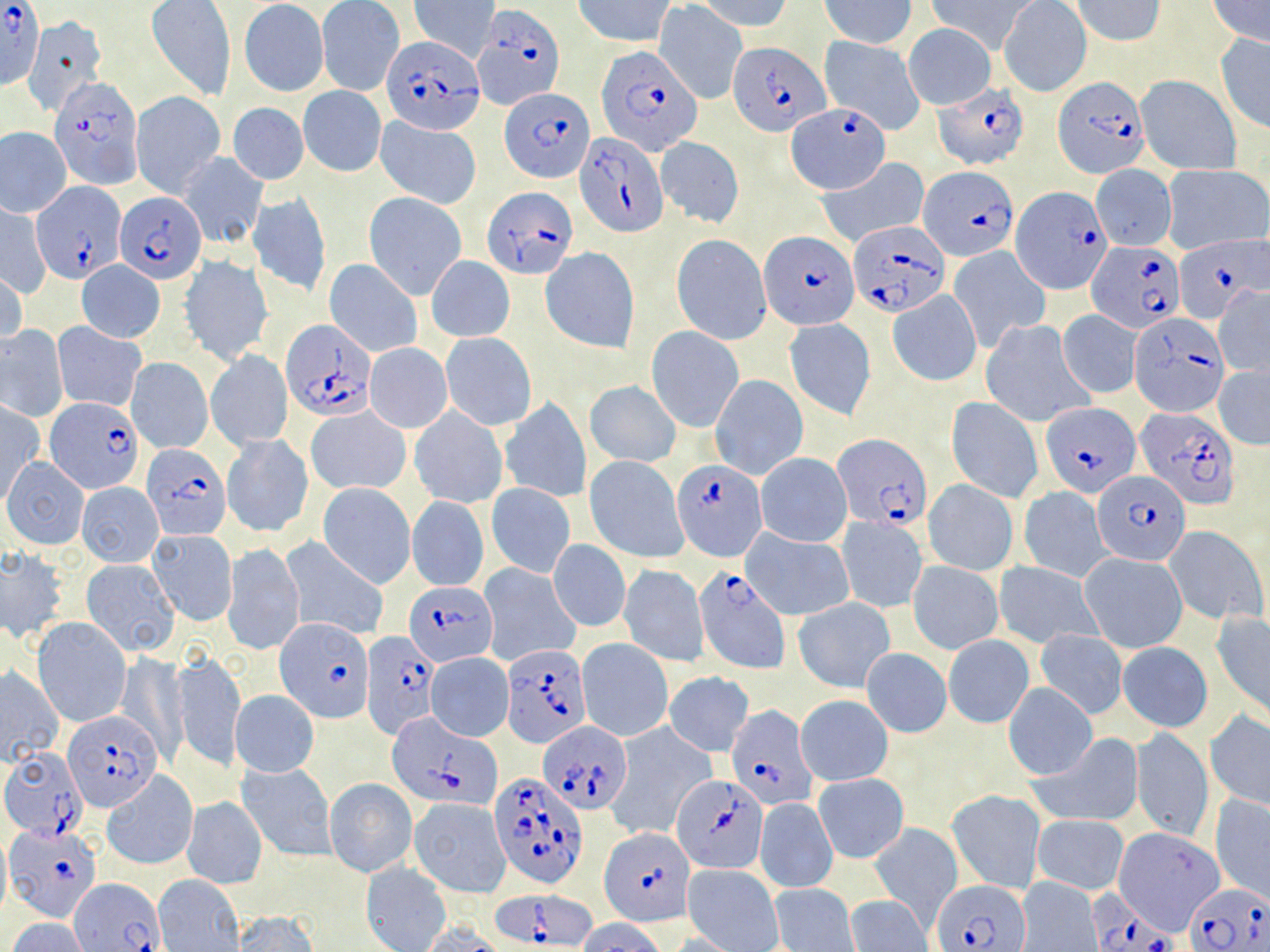
Summary:
  - Coordinate format: approximate bounding boxes as (x1,y1)-(x2,y2) corner pairs in pixels
  - Uninfected red blood cell locations (subset): (410,0)-(500,63), (572,0)-(677,48), (1071,0)-(1165,46), (1204,0)-(1270,48), (696,1)-(793,34), (822,1)-(917,48), (926,1)-(1038,55), (998,1)-(1092,97), (147,2)-(236,101), (240,2)-(329,96), (316,2)-(403,96), (656,4)-(748,104), (23,15)-(108,116), (903,24)-(996,110), (1214,33)-(1270,134), (820,35)-(926,134), (1137,74)-(1242,173), (298,86)-(386,177), (130,91)-(226,199), (228,102)-(308,186), (377,117)-(480,208), (1,127)-(71,215), (655,135)-(745,227), (178,152)-(268,249), (816,158)-(929,247), (1162,163)-(1269,255), (1090,164)-(1175,251), (248,192)-(331,298), (364,192)-(466,300), (1,204)-(51,299), (672,233)-(771,344), (540,246)-(638,353), (949,246)-(1050,348), (181,255)-(272,365), (427,258)-(514,342), (324,259)-(423,358), (76,260)-(165,344), (0,267)-(26,355), (1214,284)-(1270,379), (888,291)-(981,386), (1057,310)-(1142,397), (784,319)-(875,420), (981,319)-(1095,428), (53,323)-(145,411), (0,326)-(68,422), (646,326)-(743,432), (440,332)-(537,429), (365,343)-(452,433), (205,350)-(292,451), (126,357)-(213,454), (1213,365)-(1270,450), (710,374)-(808,482), (585,380)-(681,468), (499,396)-(591,503), (946,396)-(1043,503), (1,402)-(43,505), (306,406)-(410,495), (410,407)-(507,509), (223,435)-(312,536), (756,453)-(852,547), (585,455)-(688,563), (1,456)-(88,549), (923,480)-(1017,576), (76,483)-(163,566), (318,483)-(416,588), (485,484)-(574,579), (1019,486)-(1111,582), (408,496)-(489,592), (837,515)-(927,615), (1164,525)-(1267,625), (148,529)-(237,625), (743,529)-(855,621), (281,536)-(390,643), (548,539)-(630,634), (223,542)-(305,656), (0,546)-(68,645), (1080,551)-(1189,653), (80,558)-(181,656), (908,561)-(1003,654), (994,562)-(1099,648), (479,563)-(581,667), (619,563)-(708,666), (793,597)-(894,692), (1212,612)-(1270,724), (33,618)-(131,728), (1034,628)-(1128,719), (943,636)-(1034,728), (576,637)-(673,742), (1116,641)-(1212,732), (862,647)-(951,737), (171,648)-(245,773), (426,652)-(514,741), (116,653)-(188,765), (0,667)-(65,764), (665,671)-(754,756), (1003,684)-(1097,781), (231,690)-(319,776), (796,694)-(893,785), (1205,710)-(1270,813), (608,725)-(716,836), (1131,727)-(1213,842), (1029,734)-(1144,829), (237,762)-(336,861), (102,773)-(198,870), (815,774)-(908,863), (324,777)-(417,877), (948,789)-(1045,895), (1211,794)-(1270,904), (184,798)-(266,889), (409,798)-(511,897), (756,799)-(837,893), (1033,815)-(1129,895), (868,823)-(962,927), (1114,827)-(1227,935), (360,861)-(452,952), (683,864)-(783,951), (153,876)-(245,951), (1016,877)-(1102,951), (770,884)-(858,951), (845,895)-(933,952), (228,911)-(318,951), (8,918)-(92,952), (576,918)-(669,952), (418,921)-(505,951)
  - Plasmodium falciparum-infected red blood cell locations (subset): (0,3)-(44,87), (473,4)-(564,111), (380,35)-(481,136), (727,40)-(828,135), (598,44)-(703,156), (52,75)-(144,190), (1053,78)-(1147,180), (935,84)-(1030,170), (500,87)-(592,181), (785,106)-(889,192), (576,132)-(665,235), (921,166)-(1017,261), (34,182)-(124,282), (484,187)-(576,279), (116,191)-(206,284), (847,223)-(949,316), (760,230)-(858,328), (1174,235)-(1265,325), (1089,241)-(1183,331), (1131,313)-(1230,416), (281,321)-(376,420), (46,398)-(142,492), (1041,403)-(1142,497), (1137,407)-(1241,511), (833,435)-(931,529), (142,443)-(230,539), (672,459)-(766,560), (1092,469)-(1191,565), (695,565)-(790,674), (404,579)-(498,666), (276,617)-(376,722), (362,632)-(441,740), (503,643)-(590,746), (727,705)-(817,811), (64,710)-(164,811), (389,714)-(503,809), (538,722)-(631,813), (1,747)-(84,840), (672,774)-(769,874), (491,777)-(588,891), (5,824)-(100,920), (599,827)-(694,925), (72,880)-(164,952), (934,881)-(1030,951), (1186,881)-(1270,952), (494,891)-(596,949), (1085,891)-(1177,951)
  - Slide-level diagnosis: Plasmodium falciparum
  - Magnification: 1000x
  - Image size: 1270×952 pixels
  - Field of view: one of a larger specimen
  - Stain: May-Grünwald-Giemsa
  - Modality: light microscopy
  - Preparation: thin blood smear